Report the malaria status of this cell.
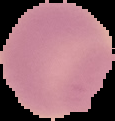
Uninfected.

image type = segmented cell region on a black background
preparation = thin blood film
image size = 115×121 pixels